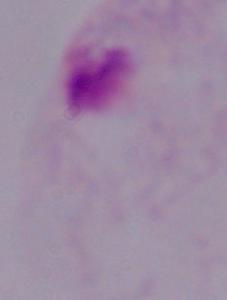
{
  "identification": "trichomonad",
  "modality": "micrograph",
  "magnification": "1000x"
}